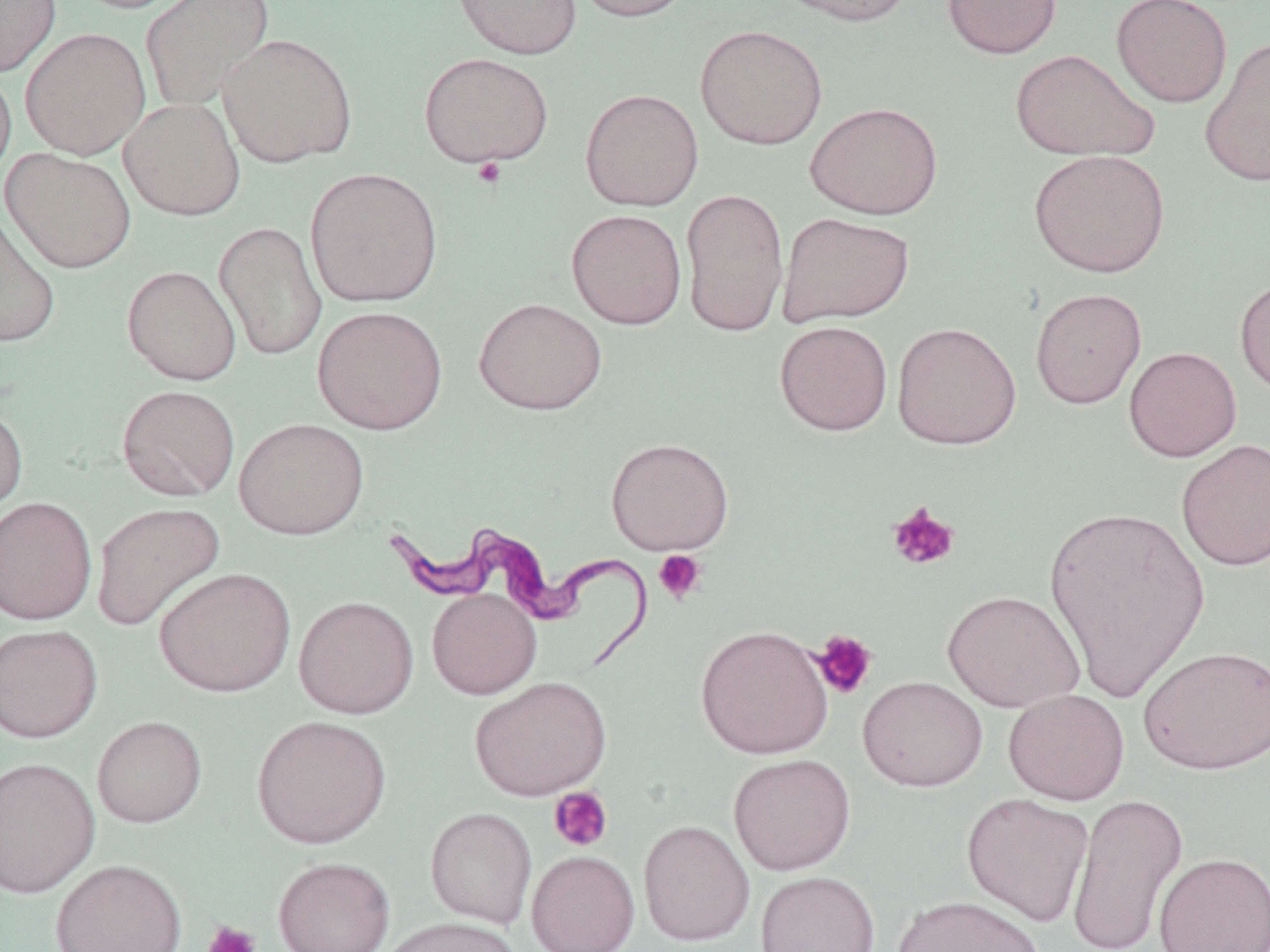

Summary:
  - Coordinate format: approximate bounding boxes as (x1, y1, x2, y2) in pixels
  - Uninfected red blood cell locations: (65, 0, 197, 14), (140, 0, 275, 114), (450, 0, 583, 60), (572, 0, 695, 23), (774, 0, 918, 27), (942, 0, 1063, 59), (1112, 0, 1232, 108), (0, 1, 61, 77), (694, 24, 828, 150), (20, 27, 151, 160), (217, 32, 358, 168), (1200, 37, 1270, 187), (1010, 49, 1160, 162), (418, 51, 554, 168), (0, 63, 16, 182), (580, 88, 704, 211), (119, 97, 245, 220), (805, 101, 943, 219), (2, 147, 136, 273), (1029, 149, 1170, 278), (304, 167, 443, 307), (680, 187, 789, 337), (0, 208, 61, 349), (566, 209, 687, 330), (777, 212, 915, 326), (214, 221, 327, 361), (122, 265, 241, 385), (1234, 275, 1270, 396), (1030, 288, 1147, 409), (473, 297, 607, 415), (312, 305, 448, 434), (774, 320, 893, 436), (891, 321, 1022, 450), (1124, 346, 1241, 461), (117, 384, 240, 501), (0, 401, 29, 522), (234, 417, 369, 539), (606, 437, 734, 555), (1176, 438, 1270, 572), (0, 496, 98, 624), (90, 501, 226, 632), (1044, 503, 1211, 702), (154, 566, 296, 697), (426, 588, 541, 699), (941, 590, 1086, 712), (293, 595, 419, 718), (0, 624, 102, 743), (695, 624, 834, 759), (1137, 645, 1270, 775), (858, 675, 988, 792), (469, 676, 612, 801), (1003, 689, 1129, 806), (252, 715, 391, 848), (91, 716, 207, 828), (728, 753, 856, 875), (0, 756, 100, 898), (961, 792, 1095, 926), (1066, 793, 1188, 952), (425, 807, 537, 928), (638, 820, 755, 946), (527, 850, 640, 952), (1153, 851, 1270, 952), (272, 856, 395, 952), (49, 859, 188, 952), (754, 870, 881, 952), (893, 894, 1044, 952), (377, 916, 523, 952)
  - Platelet locations: (472, 157, 506, 188), (887, 502, 961, 572), (653, 550, 707, 604), (810, 629, 878, 699), (549, 786, 613, 853), (202, 920, 261, 952)
  - Trypanosoma brucei locations: (391, 517, 655, 676)
  - Slide-level diagnosis: Trypanosoma brucei
  - Image size: 1270×952 pixels
  - Field of view: single
  - Magnification: 1000x
  - Modality: optical microscopy
  - Stain: May-Grünwald-Giemsa
  - Preparation: thin blood film